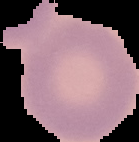

Summary:
  - Image size: 139×142 pixels
  - Image type: cell region segmented out of the field of view; surrounding area masked to black
  - Preparation: thin blood film
  - Malaria status: uninfected